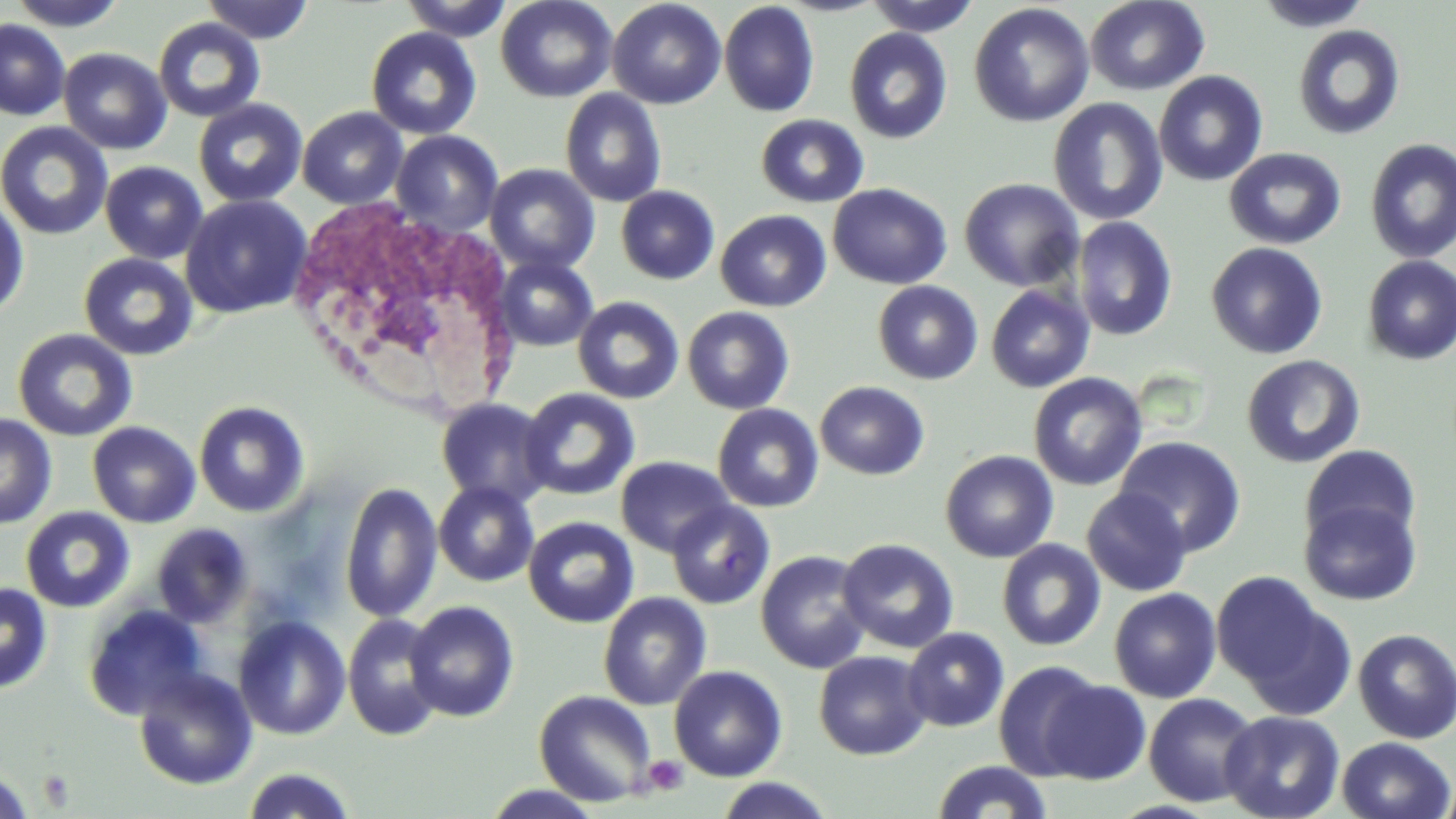
{
  "slide_level_diagnosis": "no evidence of blood parasites",
  "uninfected_red_blood_cell_locations": "approximate bounding boxes as named x1/y1/x2/y2 corners in pixels: (x1=6, y1=0, x2=132, y2=31), (x1=200, y1=0, x2=315, y2=44), (x1=399, y1=0, x2=512, y2=41), (x1=495, y1=0, x2=618, y2=103), (x1=607, y1=0, x2=726, y2=109), (x1=862, y1=0, x2=982, y2=36), (x1=1085, y1=0, x2=1210, y2=95), (x1=1254, y1=0, x2=1373, y2=32), (x1=719, y1=1, x2=820, y2=118), (x1=969, y1=3, x2=1095, y2=127), (x1=153, y1=18, x2=266, y2=123), (x1=0, y1=19, x2=70, y2=121), (x1=1292, y1=25, x2=1406, y2=141), (x1=366, y1=27, x2=482, y2=140), (x1=844, y1=27, x2=953, y2=144), (x1=58, y1=48, x2=172, y2=154), (x1=1153, y1=70, x2=1268, y2=187), (x1=559, y1=88, x2=668, y2=207), (x1=1047, y1=97, x2=1168, y2=226), (x1=193, y1=98, x2=308, y2=208), (x1=298, y1=107, x2=408, y2=209), (x1=755, y1=114, x2=870, y2=208), (x1=0, y1=121, x2=113, y2=241), (x1=391, y1=130, x2=503, y2=235), (x1=1364, y1=138, x2=1456, y2=263), (x1=1224, y1=148, x2=1346, y2=249), (x1=100, y1=161, x2=208, y2=264), (x1=484, y1=163, x2=600, y2=275), (x1=958, y1=178, x2=1084, y2=292), (x1=827, y1=183, x2=952, y2=290), (x1=615, y1=186, x2=720, y2=285), (x1=0, y1=194, x2=31, y2=322), (x1=180, y1=194, x2=312, y2=318), (x1=715, y1=209, x2=831, y2=312), (x1=1071, y1=216, x2=1178, y2=341), (x1=1206, y1=242, x2=1328, y2=360), (x1=78, y1=253, x2=199, y2=361), (x1=493, y1=255, x2=599, y2=351), (x1=1361, y1=255, x2=1456, y2=365), (x1=872, y1=281, x2=983, y2=384), (x1=985, y1=284, x2=1095, y2=393), (x1=572, y1=296, x2=685, y2=404), (x1=682, y1=306, x2=795, y2=414), (x1=12, y1=328, x2=139, y2=442), (x1=1241, y1=354, x2=1365, y2=469), (x1=1028, y1=372, x2=1148, y2=491), (x1=814, y1=381, x2=929, y2=480), (x1=519, y1=387, x2=640, y2=501), (x1=435, y1=397, x2=554, y2=509), (x1=194, y1=400, x2=310, y2=517), (x1=712, y1=404, x2=824, y2=512), (x1=0, y1=413, x2=58, y2=529), (x1=87, y1=421, x2=201, y2=528), (x1=1114, y1=436, x2=1247, y2=556), (x1=1299, y1=444, x2=1421, y2=551), (x1=940, y1=449, x2=1058, y2=563), (x1=615, y1=455, x2=735, y2=557), (x1=433, y1=480, x2=540, y2=587), (x1=340, y1=481, x2=444, y2=623), (x1=1081, y1=488, x2=1192, y2=596), (x1=1299, y1=498, x2=1421, y2=606), (x1=666, y1=500, x2=775, y2=610), (x1=21, y1=506, x2=135, y2=613), (x1=523, y1=516, x2=639, y2=628), (x1=151, y1=524, x2=254, y2=628), (x1=1094, y1=530, x2=1210, y2=670), (x1=837, y1=537, x2=959, y2=654), (x1=996, y1=539, x2=1106, y2=651), (x1=755, y1=550, x2=872, y2=673), (x1=1211, y1=571, x2=1344, y2=704), (x1=0, y1=581, x2=53, y2=694), (x1=1108, y1=587, x2=1222, y2=703), (x1=598, y1=592, x2=712, y2=710), (x1=404, y1=600, x2=520, y2=723), (x1=81, y1=603, x2=211, y2=721), (x1=343, y1=614, x2=446, y2=741), (x1=233, y1=615, x2=351, y2=741), (x1=902, y1=627, x2=1010, y2=732), (x1=1353, y1=628, x2=1456, y2=744), (x1=813, y1=651, x2=932, y2=760), (x1=994, y1=661, x2=1104, y2=780), (x1=668, y1=665, x2=787, y2=782), (x1=132, y1=667, x2=258, y2=790), (x1=1040, y1=679, x2=1151, y2=784), (x1=534, y1=690, x2=657, y2=807), (x1=1143, y1=692, x2=1262, y2=807), (x1=1219, y1=710, x2=1345, y2=819), (x1=1337, y1=736, x2=1454, y2=819), (x1=931, y1=760, x2=1053, y2=818), (x1=241, y1=766, x2=359, y2=818), (x1=0, y1=767, x2=37, y2=817), (x1=713, y1=777, x2=835, y2=819), (x1=1438, y1=778, x2=1456, y2=819), (x1=481, y1=784, x2=605, y2=819)",
  "field_of_view": "single",
  "white_blood_cell_locations": "approximate bounding boxes as named x1/y1/x2/y2 corners in pixels: (x1=295, y1=200, x2=517, y2=414)",
  "preparation": "thin blood film",
  "platelet_locations": "approximate bounding boxes as named x1/y1/x2/y2 corners in pixels: (x1=642, y1=755, x2=689, y2=796), (x1=37, y1=769, x2=75, y2=809)",
  "modality": "light microscopy",
  "image_size": "1456×819 pixels",
  "magnification": "1000x",
  "stain": "May-Grünwald-Giemsa"
}